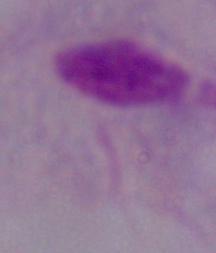 A trichomonad is seen. Micrograph. Captured at 1000x magnification.